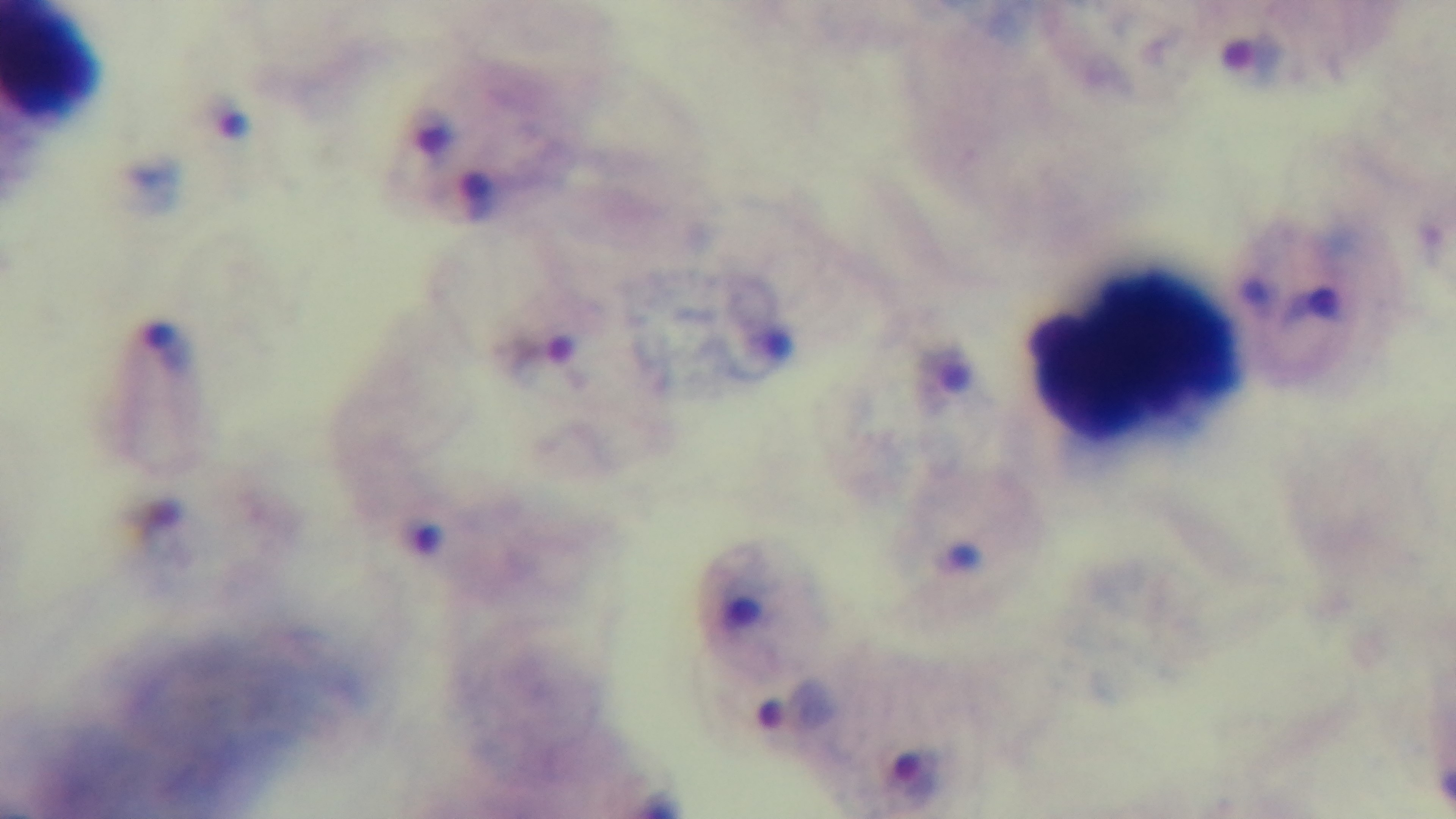

Summary:
  - Capture: mounted 4K digital camera
  - Field of view: single
  - Objective: 100x oil immersion
  - Modality: light microscopy
  - Malaria status: infected
  - Stain: Giemsa
  - Preparation: thick blood film